Report the malaria status of this cell.
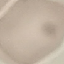

Uninfected.

stain: Giemsa
preparation: thin blood smear
image_type: automatically extracted cell patch, resized to 64 × 64 pixels
capture: smartphone camera at the microscope eyepiece